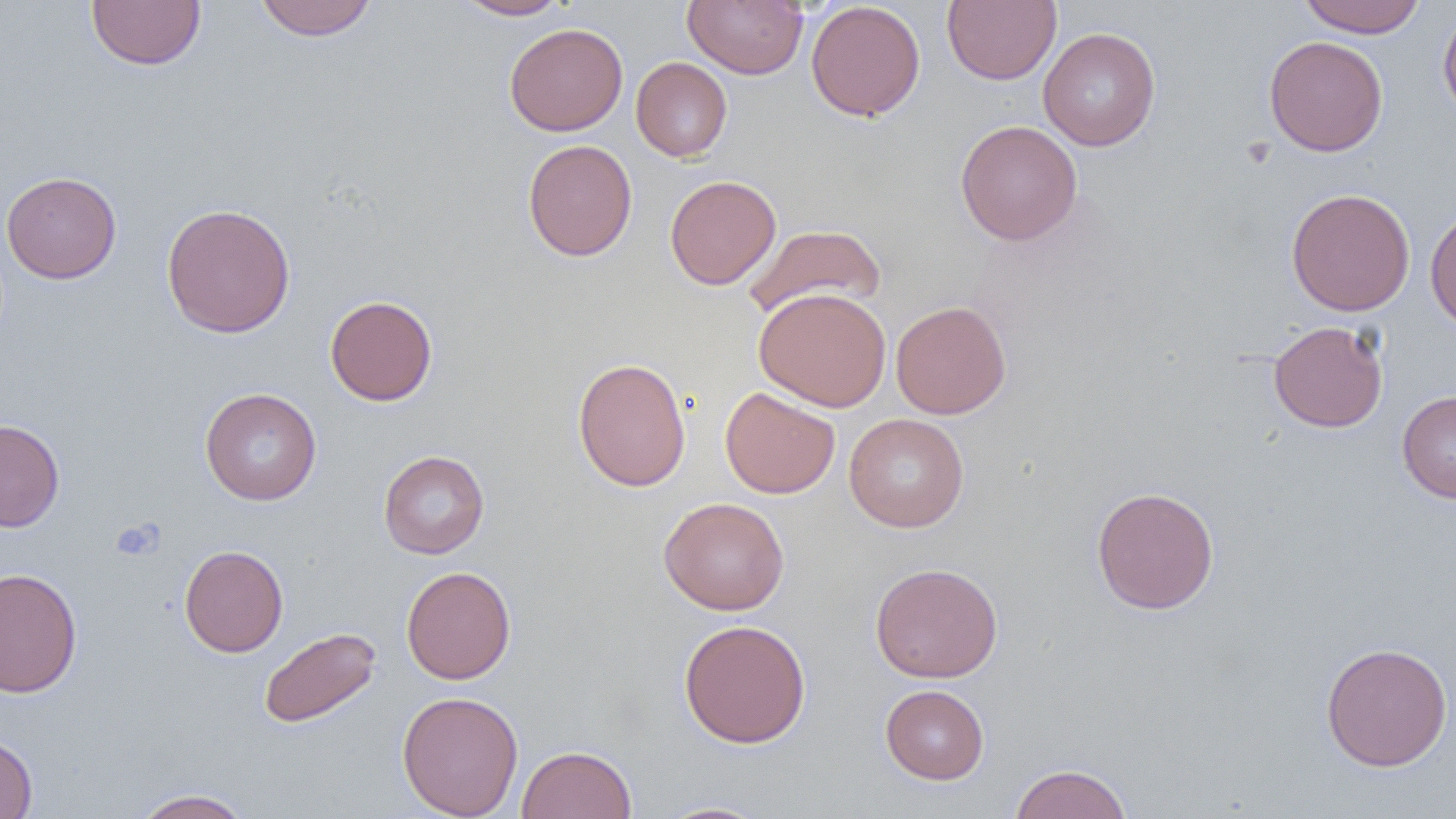

Summary:
  - Coordinate format: approximate bounding boxes as (x1, y1, x2, y2) in pixels
  - Platelet locations: (112, 519, 163, 560)
  - Uninfected red blood cell locations: (86, 0, 206, 71), (253, 0, 379, 41), (454, 0, 572, 20), (683, 0, 808, 79), (942, 0, 1061, 85), (1297, 0, 1427, 37), (805, 1, 926, 121), (1437, 5, 1456, 123), (504, 22, 628, 136), (1038, 27, 1161, 151), (1263, 35, 1388, 157), (631, 57, 732, 162), (956, 120, 1083, 246), (522, 139, 638, 261), (1, 171, 121, 283), (665, 174, 781, 290), (1286, 188, 1415, 316), (160, 202, 296, 338), (1425, 203, 1456, 332), (742, 224, 887, 323), (754, 288, 892, 412), (325, 294, 438, 406), (890, 300, 1011, 419), (1268, 320, 1388, 432), (573, 357, 691, 492), (720, 386, 840, 498), (199, 387, 322, 505), (1397, 390, 1456, 503), (844, 413, 969, 532), (0, 418, 65, 532), (378, 450, 489, 559), (1091, 486, 1220, 615), (658, 497, 790, 615), (179, 544, 288, 657), (869, 561, 1003, 683), (401, 565, 516, 685), (0, 567, 82, 698), (678, 619, 811, 748), (258, 626, 381, 729), (1321, 642, 1453, 771), (880, 684, 989, 784), (396, 690, 524, 818), (0, 732, 38, 818), (517, 745, 636, 819), (1009, 762, 1132, 819), (131, 789, 256, 818), (654, 800, 773, 819)
  - Slide-level diagnosis: negative for blood parasites
  - Field of view: single
  - Modality: optical microscopy
  - Preparation: thin blood film
  - Image size: 1456×819 pixels
  - Magnification: 1000x